Assess this cell for malaria.
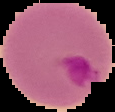

Parasitized.

Cell region segmented out of the field of view; the surrounding area is masked to black. From a thin blood film. Image is 115×112 pixels.